Classify this cell by malaria status.
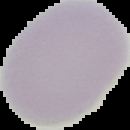
It is uninfected.

image type = cell region segmented out of the field of view; surrounding area masked to black
preparation = thin blood film
image size = 130×130 pixels